Locate every Plasmodium vivax-infected red blood cell.
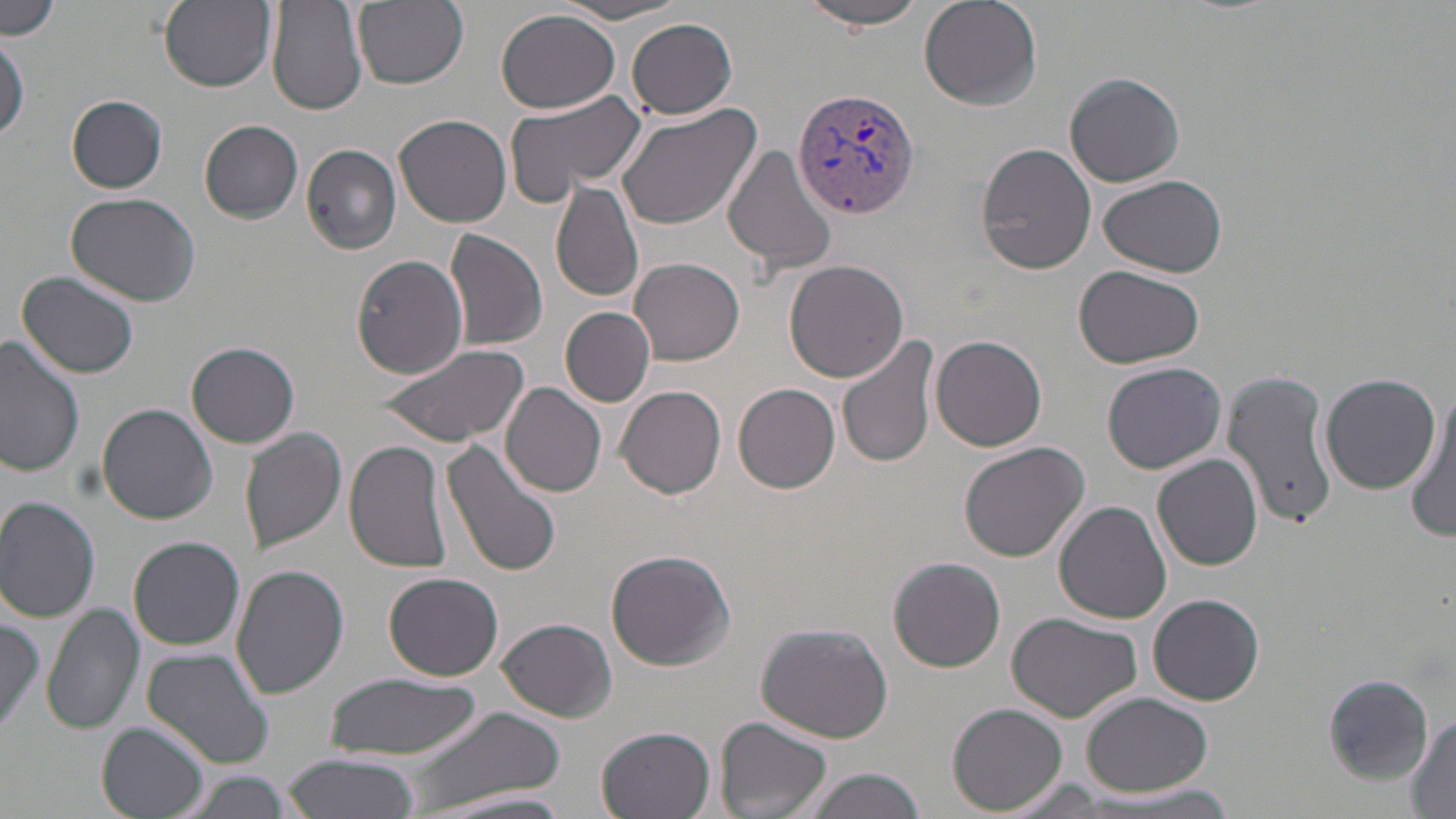

Approximate bounding boxes as (x1, y1, x2, y2) in pixels.
Plasmodium vivax-infected red blood cells: (793, 86, 922, 217).

Uninfected red blood cell locations: (156, 0, 276, 92), (268, 0, 368, 116), (351, 0, 469, 90), (919, 0, 1041, 110), (1, 1, 67, 37), (798, 1, 929, 32), (556, 2, 695, 25), (495, 9, 620, 114), (626, 18, 737, 120), (0, 37, 27, 140), (1064, 72, 1186, 187), (502, 89, 651, 201), (66, 95, 168, 193), (614, 102, 762, 230), (393, 112, 512, 227), (201, 119, 303, 221), (977, 140, 1097, 275), (723, 143, 838, 280), (301, 144, 404, 255), (1098, 174, 1227, 278), (550, 180, 645, 304), (66, 193, 201, 307), (444, 228, 547, 352), (353, 253, 471, 378), (631, 257, 744, 364), (784, 260, 911, 385), (1073, 264, 1205, 369), (16, 271, 141, 380), (560, 307, 656, 406), (836, 333, 938, 470), (930, 335, 1048, 453), (0, 337, 85, 477), (187, 341, 299, 448), (376, 342, 531, 449), (1101, 362, 1227, 475), (1222, 366, 1339, 531), (1319, 371, 1442, 496), (501, 382, 606, 497), (734, 384, 841, 494), (615, 385, 727, 499), (1408, 391, 1455, 542), (97, 403, 217, 524), (239, 428, 348, 553), (345, 438, 454, 573), (440, 438, 562, 578), (958, 441, 1091, 566), (1152, 454, 1264, 571), (0, 496, 101, 623), (1056, 500, 1173, 623), (130, 536, 244, 651), (605, 549, 735, 670), (889, 556, 1006, 673), (231, 564, 350, 700), (382, 572, 504, 680), (1149, 593, 1265, 706), (44, 603, 145, 736), (1006, 612, 1142, 721), (0, 613, 48, 734), (497, 618, 617, 722), (756, 622, 892, 743), (140, 649, 273, 768), (324, 673, 484, 762), (1322, 673, 1432, 782), (1081, 692, 1215, 796), (948, 703, 1070, 816), (405, 704, 568, 816), (1409, 713, 1455, 817), (715, 718, 834, 819), (96, 720, 209, 819), (596, 727, 716, 819), (283, 754, 419, 819), (796, 766, 927, 819), (176, 771, 297, 819), (1075, 781, 1246, 817), (419, 789, 576, 819). Slide-level diagnosis: Plasmodium vivax. Light microscopy. Single field of view. 1000x magnification. May-Grünwald-Giemsa stain. Thin blood film. Image is 1456×819 pixels.